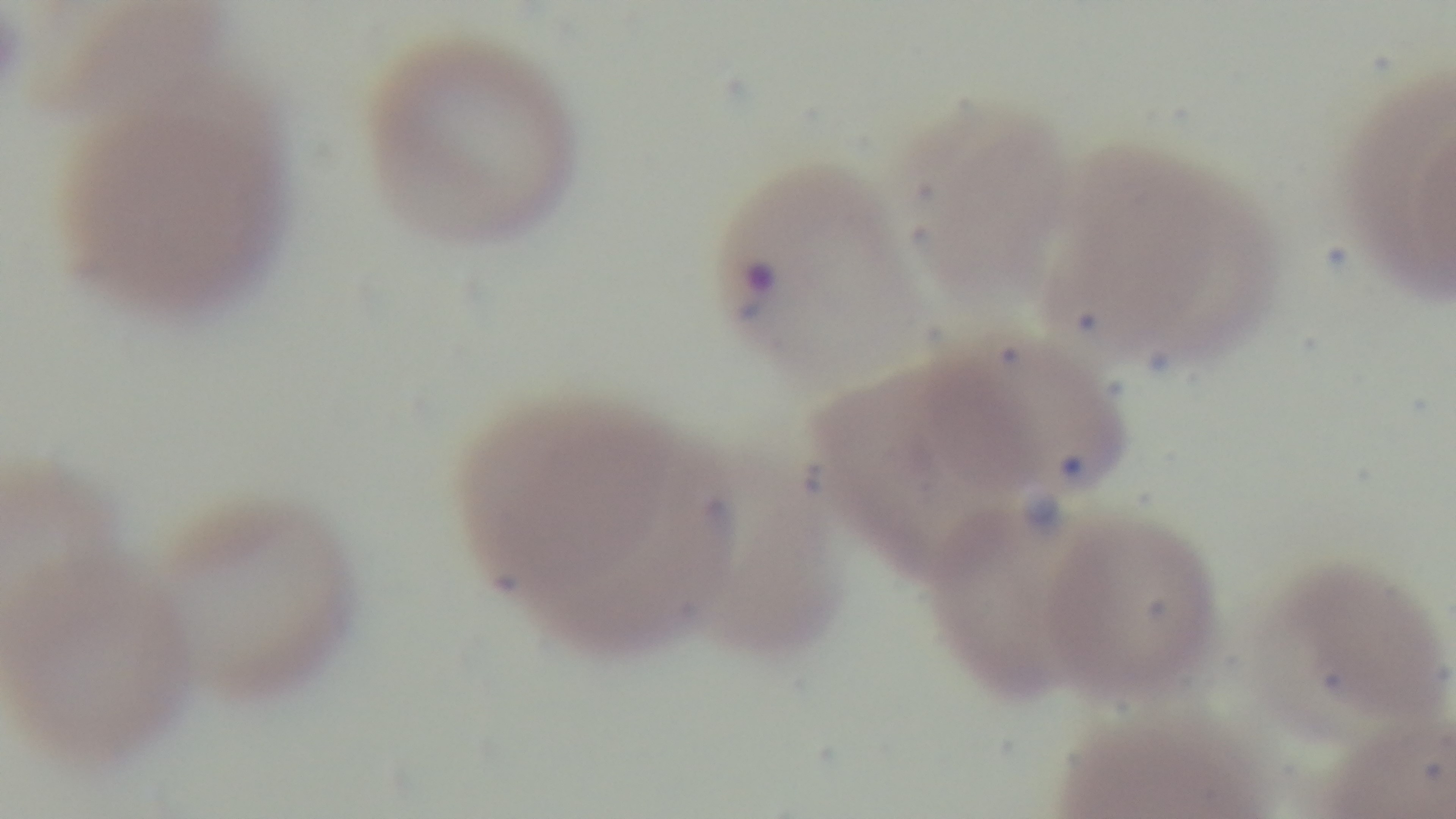

Malaria status: positive. Giemsa-stained. Mounted 4K digital camera. Oil-immersion objective, 100x. Preparation: thin. Photomicrograph. Single field of view.